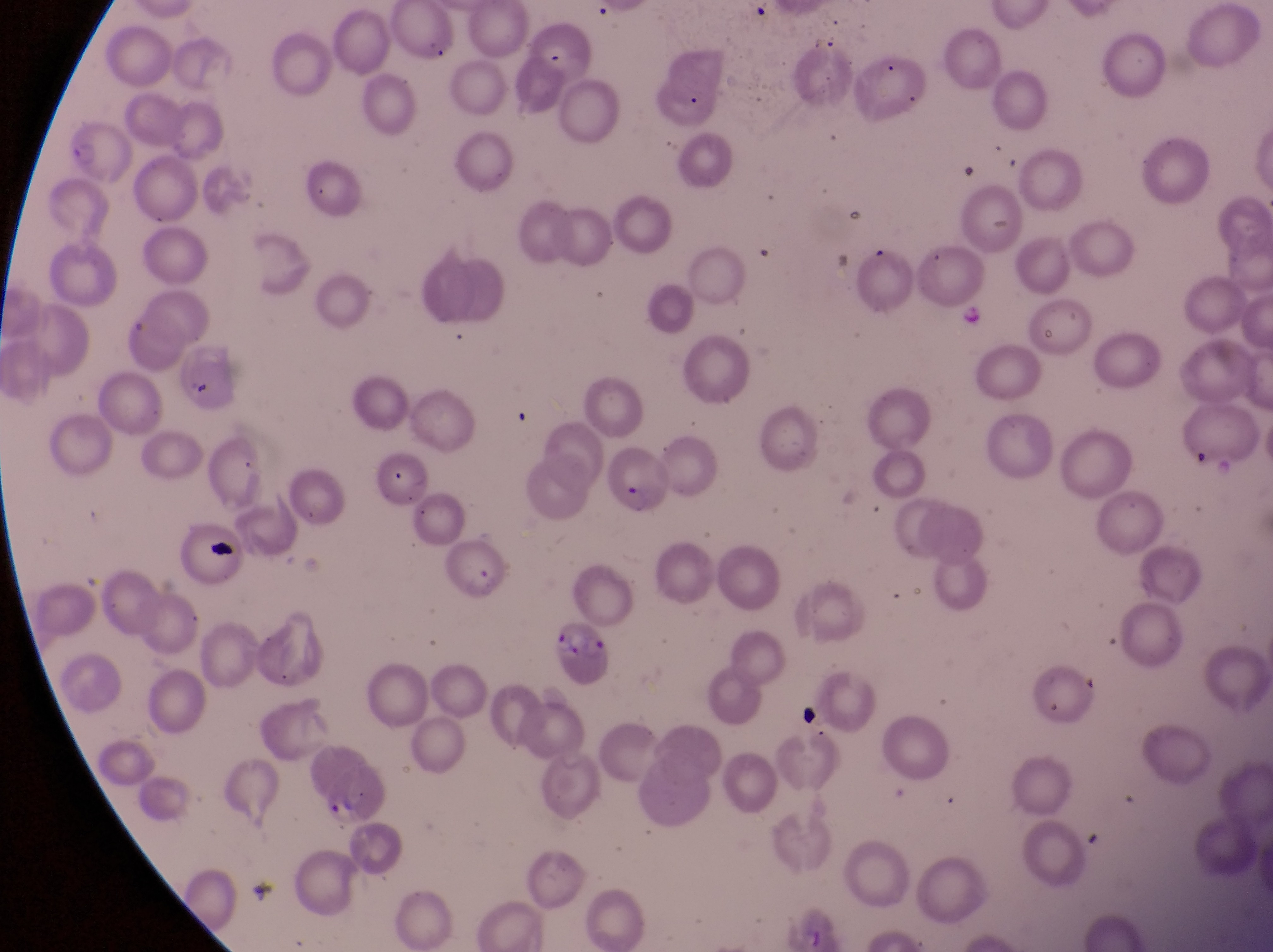

parasitised red blood cell locations = approximate bounding boxes as [left, top, right, bottom] in pixels: [606, 445, 669, 520], [537, 619, 607, 693]
country = Uganda
magnification = 1000x
capture = smartphone photograph through the eyepiece of an Olympus CX-23 microscope
field of view = single
preparation = thin blood smear
image size = 1273×952 pixels
artifact (platelet-like body, stain precipitate, or debris) locations = approximate bounding boxes as [left, top, right, bottom] in pixels: [202, 537, 242, 565], [801, 700, 823, 733]